Report the malaria status of this cell.
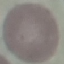
Uninfected.

{
  "preparation": "thin blood film",
  "image_type": "cell patch, automatically extracted from a larger field of view and resized to 64 × 64 pixels",
  "capture": "smartphone camera at the microscope eyepiece",
  "stain": "Giemsa"
}